Assess this cell for malaria.
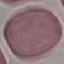

It is uninfected.

Thin smear of blood. Acquired by smartphone through the microscope eyepiece. Giemsa stain. Cell patch, automatically extracted from a larger field of view and resized to 64 × 64 pixels.